Classify this cell by malaria status.
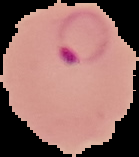
It is parasitized.

Summary:
  - Image size: 139×157 pixels
  - Preparation: thin blood film
  - Image type: segmented cell region on a black background